Describe the morphology of the erythrocytes.
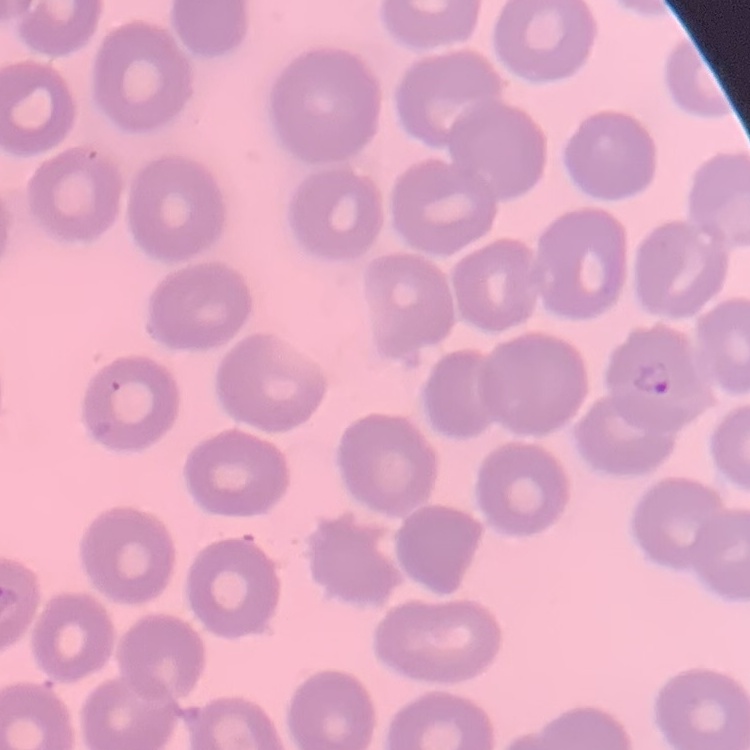
No rouleaux formation.

Square crop of a larger photomicrograph. Stained with either Field's or Giemsa. Thin blood film.